Locate every malaria parasite.
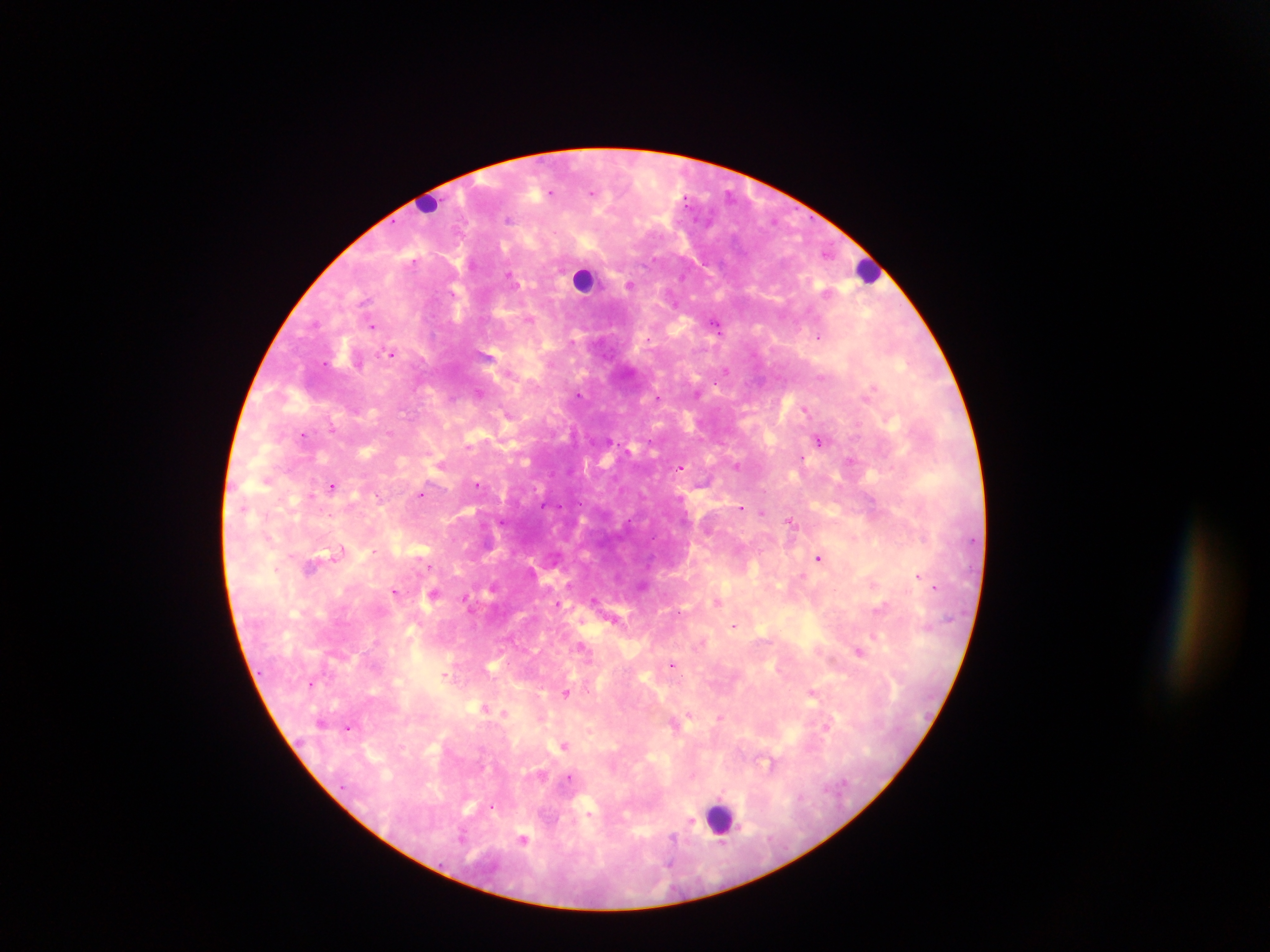

Approximate centers as [x, y] in pixels.
Malaria parasites: [592, 193], [509, 220], [511, 274], [629, 283], [365, 300], [529, 322], [715, 323], [375, 328], [819, 338], [392, 353], [487, 354], [726, 369], [873, 386], [479, 393], [579, 394], [657, 397], [806, 410], [505, 412], [391, 431], [303, 435], [608, 440], [819, 440], [803, 459], [851, 461], [439, 463], [736, 465], [680, 467], [333, 486], [478, 486], [421, 494], [873, 502], [742, 508], [763, 512], [502, 521], [790, 521], [327, 553], [339, 555], [819, 559], [430, 565], [311, 567], [917, 575], [493, 585], [875, 585], [642, 586], [935, 588], [395, 590], [434, 595], [595, 600], [719, 601], [882, 607], [614, 619], [734, 625], [583, 647], [862, 652], [832, 659], [672, 662], [493, 665], [446, 675], [451, 679], [314, 685], [814, 692], [566, 693], [487, 711], [505, 714], [690, 716], [719, 719], [828, 724], [348, 726], [564, 744], [768, 764], [569, 779], [493, 806], [692, 824], [463, 836], [674, 836], [524, 838], [672, 863].

Leukocyte locations: [426, 203], [868, 273], [583, 281], [715, 817]. Image is 1270×952 pixels. Thick blood smear. Mobile-phone photograph taken through the microscope. Single field of view. Collected in Ghana.